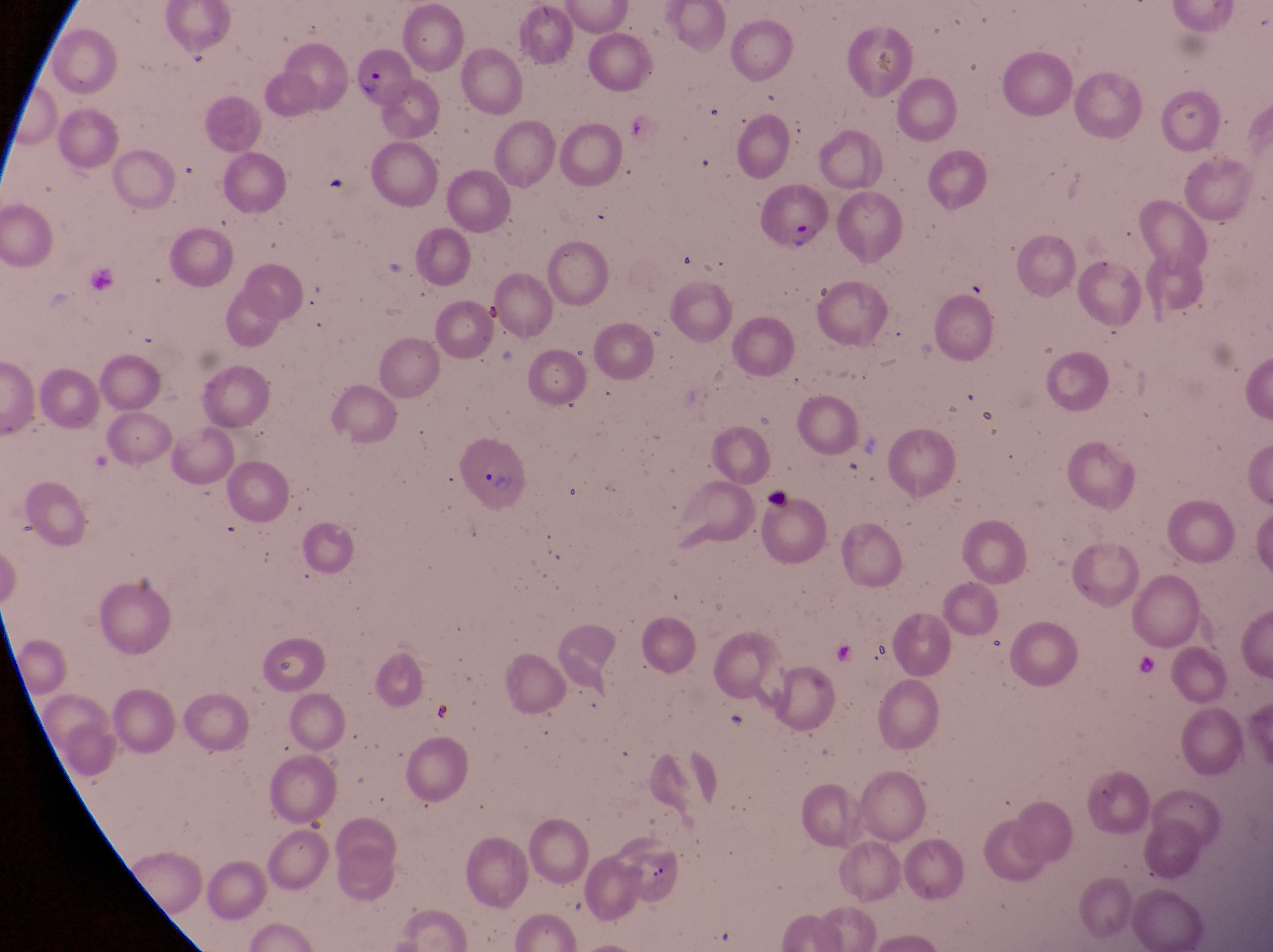

Approximate bounding boxes as left top right bottom in pixels.
Summary:
  - Parasitised red blood cell locations: 354 46 414 107; 761 182 831 260; 459 439 531 509
  - Artifact (platelet-like body, stain precipitate, or debris) locations: 642 861 687 906
  - Magnification: 1000x
  - Preparation: thin blood smear
  - Country: Uganda
  - Capture: smartphone photograph through the eyepiece of an Olympus CX-23 microscope
  - Image size: 1273×952 pixels
  - Field of view: single